Describe the morphology of the erythrocytes.
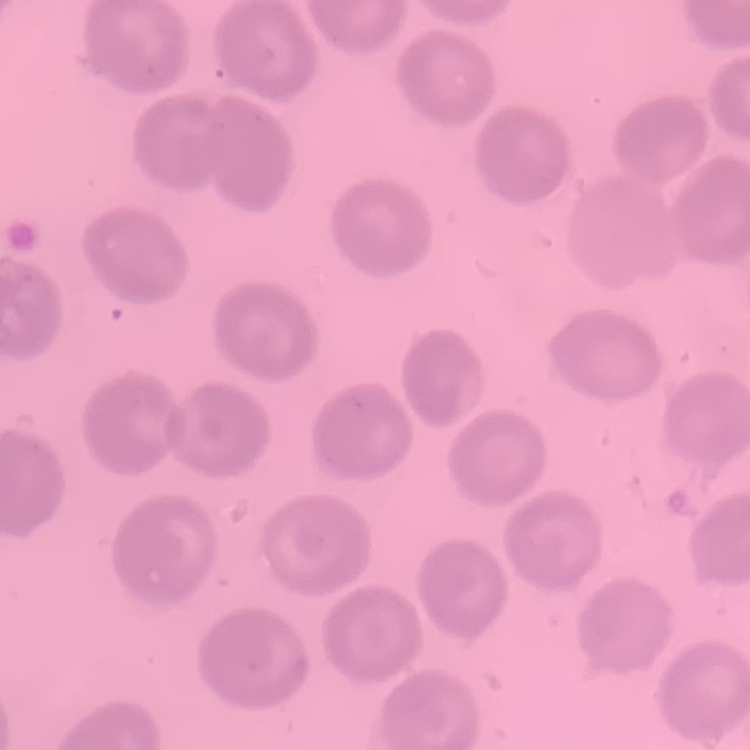
No rouleaux formation.

Summary:
  - Image type: square crop of a larger photomicrograph
  - Stain: Field's or Giemsa
  - Preparation: thin peripheral smear